Name the cell type shown.
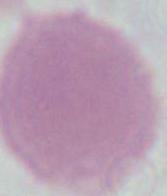

This is an erythrocyte.

{
  "magnification": "1000x",
  "modality": "micrograph"
}